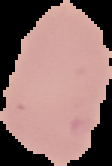

Summary:
  - Preparation: thin blood smear
  - Image type: cell region segmented out of the field of view; surrounding area masked to black
  - Image size: 112×166 pixels
  - Malaria status: uninfected